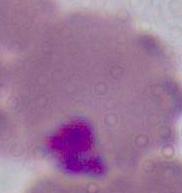
Summary:
  - Identification: Plasmodium
  - Modality: photomicrograph
  - Magnification: 400x or 1000x